Describe the morphology of the red blood cells.
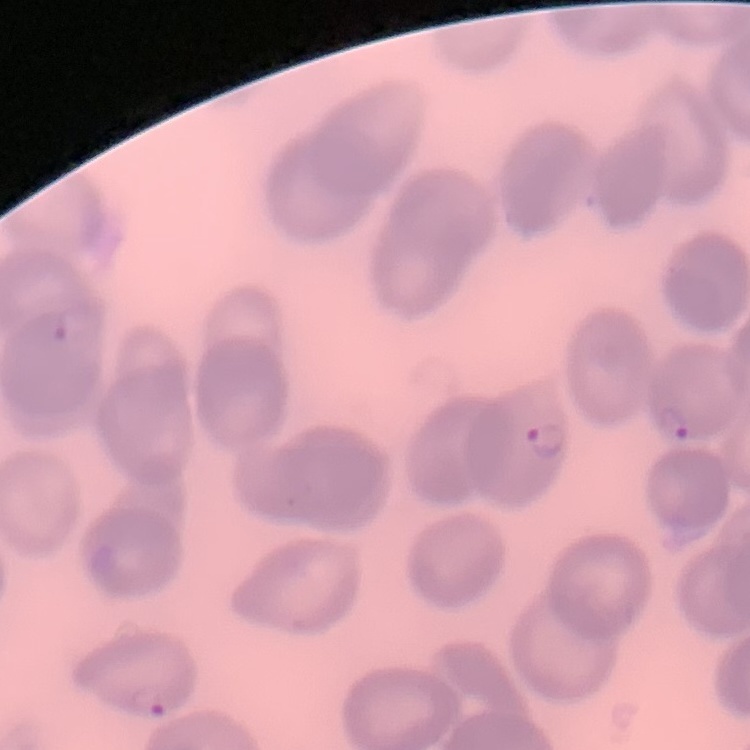
They show no rouleaux formation.

image type = square crop of a larger photomicrograph
preparation = thin blood film
stain = Field's or Giemsa